State which cell type is depicted.
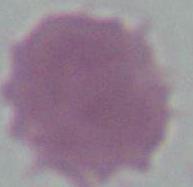

This is an erythrocyte.

1000x magnification. Photomicrograph.